Comment on the morphology of the red blood cells.
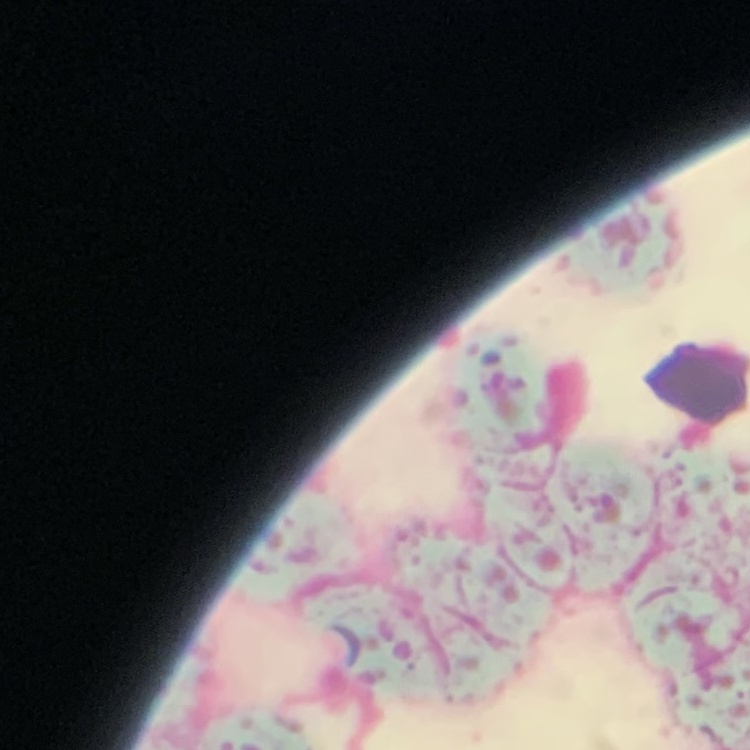

They show rouleaux formation.

Summary:
  - Image type: square crop of a larger photomicrograph
  - Stain: Field's or Giemsa
  - Preparation: thin blood film